Assess this cell for malaria.
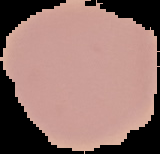
Uninfected.

image size = 160×154 pixels
preparation = thin blood film
image type = segmented cell region on a black background